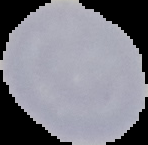 Result: no Plasmodium parasites seen. Image is 148×145 pixels. Segmented cell region on a black background. From a thin blood smear.